Give a bounding box for every trophozoite.
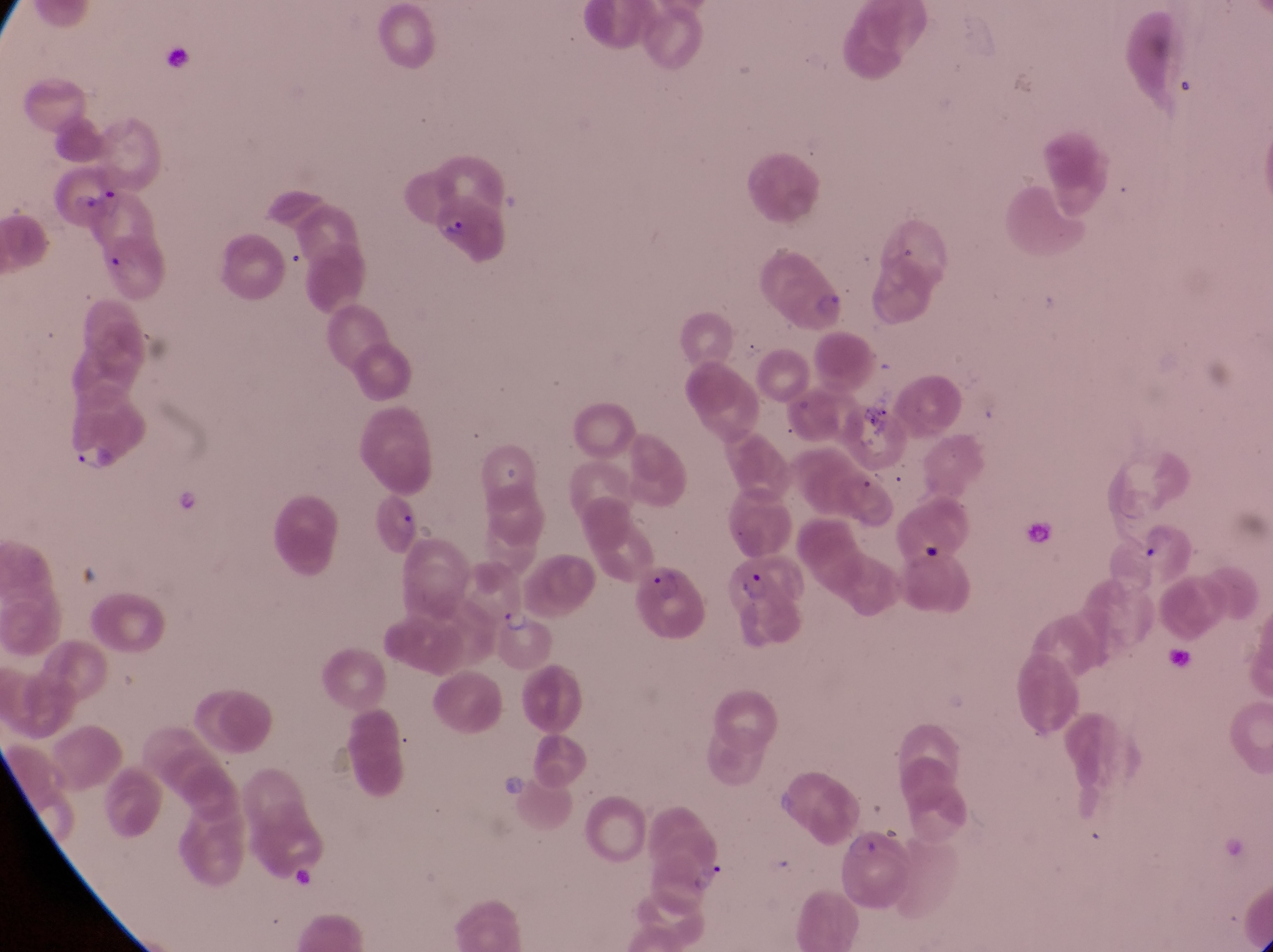

Approximate bounding boxes as (left, top, right, bottom) in pixels.
Trophozoites: (69, 440, 114, 477), (491, 600, 538, 639), (687, 859, 730, 894).

field of view = single
preparation = thin blood film
magnification = 1000x
image size = 1273×952 pixels
capture = smartphone photograph through the eyepiece of an Olympus CX-23 microscope
parasitised red blood cell locations = approximate bounding boxes as (left, top, right, bottom) in pixels: (47, 162, 124, 229), (427, 205, 514, 263), (761, 248, 851, 341), (369, 480, 426, 557), (731, 554, 813, 649), (624, 561, 709, 643), (845, 829, 912, 914)
artifact (platelet-like body, stain precipitate, or debris) locations = approximate bounding boxes as (left, top, right, bottom) in pixels: (856, 390, 898, 423), (173, 491, 200, 518), (502, 777, 521, 800), (280, 867, 320, 894)
country = Uganda